Classify this cell by malaria status.
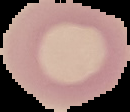
Uninfected.

Summary:
  - Image type: segmented cell region on a black background
  - Image size: 130×112 pixels
  - Preparation: thin blood film